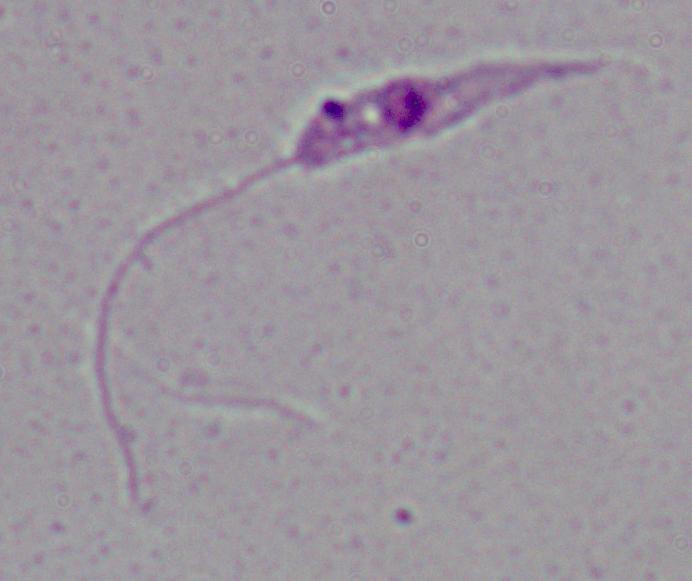
Summary:
  - Identification: Leishmania
  - Modality: micrograph
  - Magnification: 1000x